Outline each Plasmodium falciparum-infected red blood cell.
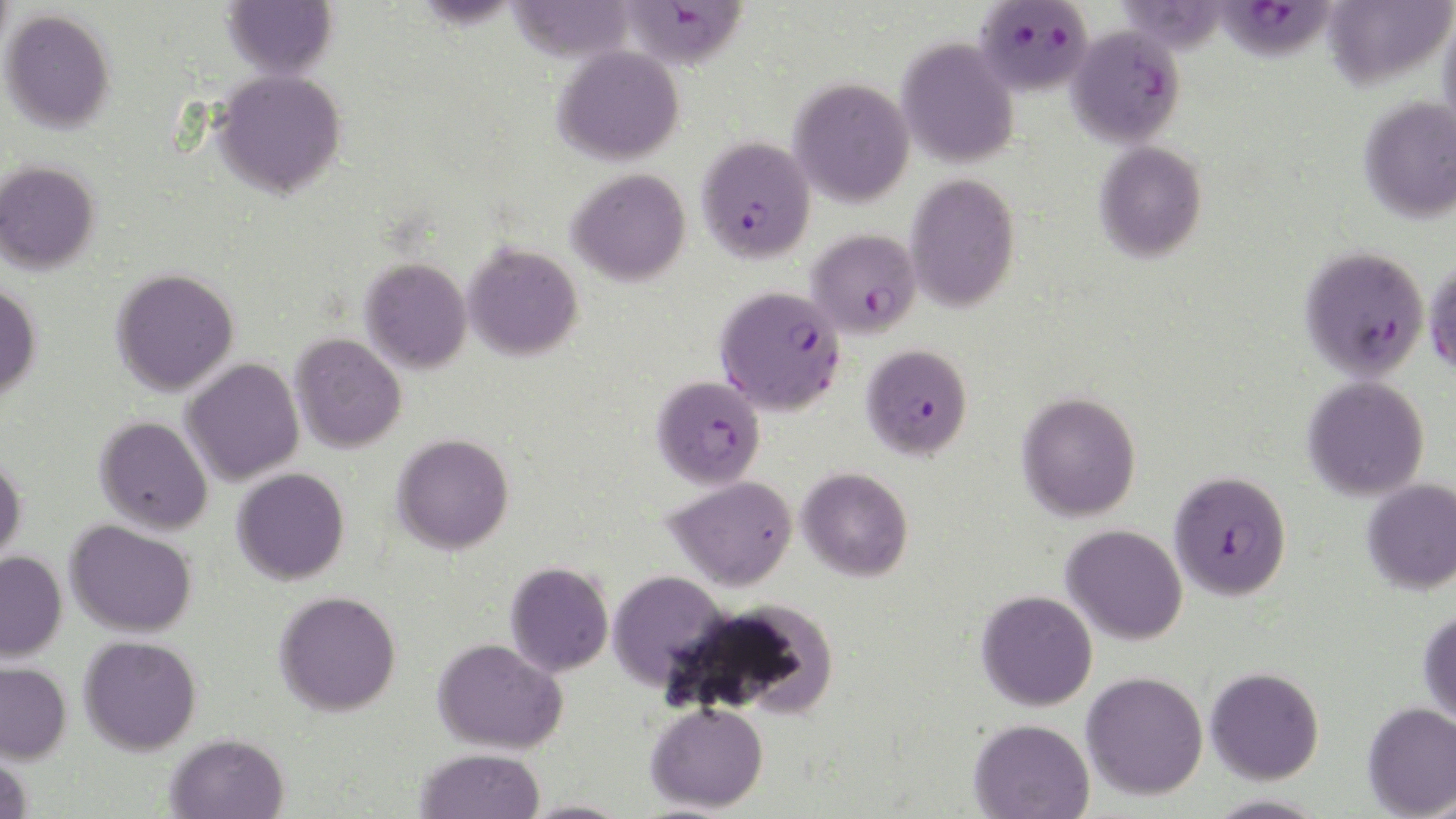

Approximate bounding boxes as (x1,y1)-(x2,y2) corner pairs in pixels.
Plasmodium falciparum-infected red blood cells: (975,1)-(1094,97), (1213,1)-(1338,63), (630,2)-(745,70), (1066,25)-(1186,148), (696,136)-(816,263), (806,229)-(921,339), (1298,245)-(1430,381), (1424,258)-(1456,377), (715,285)-(846,416), (861,343)-(973,461), (652,375)-(765,489), (1168,470)-(1293,601).

Summary:
  - Uninfected red blood cell locations: (223,0)-(338,79), (504,0)-(638,64), (1322,0)-(1455,89), (1,9)-(116,133), (1439,9)-(1456,142), (897,37)-(1019,168), (553,45)-(684,165), (211,69)-(347,198), (789,78)-(914,207), (1358,97)-(1456,223), (1094,141)-(1208,263), (0,160)-(100,274), (567,169)-(690,286), (904,172)-(1020,313), (463,243)-(583,361), (360,258)-(472,373), (111,268)-(239,397), (0,282)-(42,402), (290,333)-(406,453), (182,358)-(304,486), (1303,376)-(1429,501), (1017,391)-(1141,522), (95,416)-(213,534), (392,433)-(514,555), (0,454)-(26,566), (797,467)-(913,581), (232,468)-(349,585), (665,475)-(798,591), (1362,478)-(1456,595), (65,519)-(197,637), (1061,524)-(1187,645), (0,551)-(67,662), (505,561)-(614,676), (607,570)-(731,692), (976,590)-(1097,711), (274,591)-(401,716), (693,598)-(839,719), (1418,609)-(1456,725), (79,635)-(202,755), (433,637)-(568,754), (0,661)-(72,764), (1205,667)-(1324,784), (1081,672)-(1208,801), (644,701)-(769,813), (1362,703)-(1456,818), (968,718)-(1094,818), (165,733)-(288,819), (416,748)-(544,819), (0,752)-(33,819), (1207,794)-(1330,819), (518,800)-(635,819)
  - Slide-level diagnosis: Plasmodium falciparum
  - Magnification: 1000x
  - Image size: 1456×819 pixels
  - Preparation: thin blood smear
  - Stain: May-Grünwald-Giemsa
  - Modality: optical microscopy
  - Field of view: single